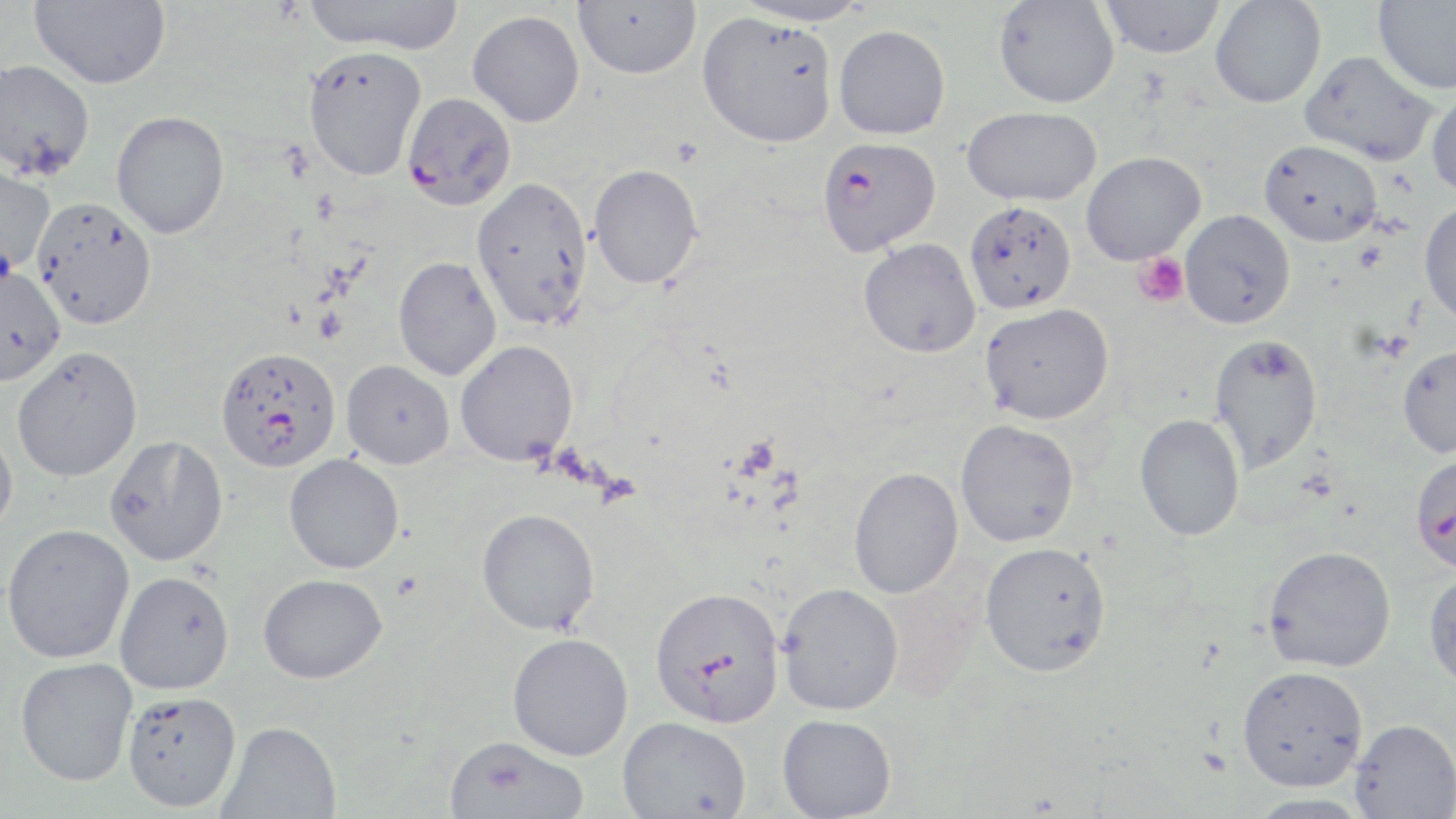 Approximate bounding boxes as named x1/y1/x2/y2 corners in pixels. Platelet locations: (x1=1132, y1=252, x2=1190, y2=307). Uninfected red blood cell locations: (x1=29, y1=0, x2=171, y2=89), (x1=304, y1=0, x2=466, y2=55), (x1=573, y1=0, x2=701, y2=79), (x1=732, y1=0, x2=873, y2=27), (x1=1373, y1=0, x2=1456, y2=94), (x1=993, y1=1, x2=1120, y2=108), (x1=1100, y1=1, x2=1226, y2=58), (x1=1210, y1=1, x2=1326, y2=109), (x1=467, y1=10, x2=585, y2=127), (x1=697, y1=11, x2=838, y2=148), (x1=834, y1=25, x2=950, y2=140), (x1=302, y1=44, x2=428, y2=181), (x1=1300, y1=50, x2=1439, y2=167), (x1=0, y1=59, x2=95, y2=180), (x1=1426, y1=86, x2=1456, y2=199), (x1=962, y1=105, x2=1101, y2=206), (x1=111, y1=110, x2=230, y2=238), (x1=1259, y1=140, x2=1383, y2=247), (x1=1081, y1=151, x2=1205, y2=265), (x1=0, y1=162, x2=55, y2=277), (x1=588, y1=164, x2=703, y2=289), (x1=471, y1=176, x2=594, y2=332), (x1=32, y1=196, x2=158, y2=329), (x1=964, y1=201, x2=1077, y2=314), (x1=1418, y1=202, x2=1456, y2=328), (x1=1179, y1=209, x2=1296, y2=329), (x1=858, y1=237, x2=982, y2=358), (x1=393, y1=256, x2=502, y2=381), (x1=0, y1=263, x2=65, y2=385), (x1=980, y1=303, x2=1114, y2=425), (x1=1208, y1=333, x2=1323, y2=473), (x1=455, y1=340, x2=578, y2=466), (x1=1397, y1=343, x2=1456, y2=458), (x1=11, y1=346, x2=143, y2=483), (x1=341, y1=360, x2=455, y2=469), (x1=1134, y1=414, x2=1245, y2=541), (x1=955, y1=419, x2=1080, y2=548), (x1=0, y1=430, x2=18, y2=539), (x1=104, y1=434, x2=229, y2=566), (x1=284, y1=454, x2=404, y2=573), (x1=848, y1=466, x2=964, y2=599), (x1=476, y1=508, x2=600, y2=634), (x1=1, y1=523, x2=135, y2=664), (x1=979, y1=541, x2=1112, y2=677), (x1=1262, y1=545, x2=1396, y2=672), (x1=115, y1=571, x2=235, y2=695), (x1=1423, y1=571, x2=1456, y2=691), (x1=258, y1=573, x2=387, y2=683), (x1=777, y1=582, x2=903, y2=715), (x1=507, y1=632, x2=634, y2=761), (x1=15, y1=657, x2=138, y2=786), (x1=1237, y1=664, x2=1368, y2=790), (x1=122, y1=691, x2=242, y2=812), (x1=777, y1=714, x2=897, y2=818), (x1=618, y1=715, x2=751, y2=818), (x1=1349, y1=718, x2=1456, y2=818), (x1=218, y1=720, x2=341, y2=818), (x1=443, y1=735, x2=589, y2=819), (x1=1243, y1=793, x2=1377, y2=819). Plasmodium falciparum-infected red blood cell locations: (x1=401, y1=91, x2=517, y2=211), (x1=816, y1=135, x2=941, y2=257), (x1=215, y1=346, x2=341, y2=472), (x1=1409, y1=452, x2=1456, y2=575), (x1=649, y1=586, x2=785, y2=728). Slide-level diagnosis: Plasmodium falciparum. One field of a larger specimen. Captured at 1000x magnification. Thin blood smear. Light microscopy. Image is 1456×819 pixels. May-Grünwald-Giemsa stain.